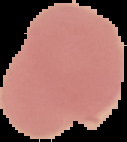

Result: negative for malaria parasites. Image is 127×142 pixels. The area outside the segmented cell region is set to black. From a thin blood film.